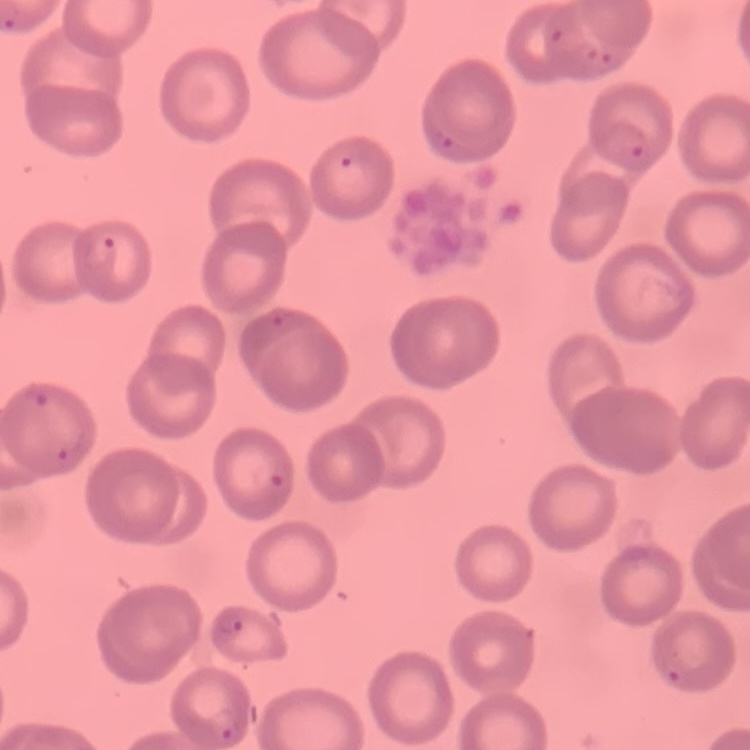
{
  "erythrocyte_morphology": "no rouleaux formation",
  "image_type": "square crop of a larger photomicrograph",
  "stain": "Field's or Giemsa",
  "preparation": "thin peripheral smear"
}